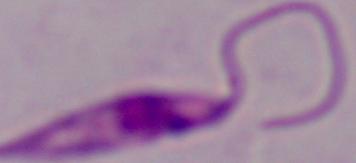

Micrograph. A Leishmania parasite is seen. Captured at 1000x magnification.